Point out each Plasmodium parasite.
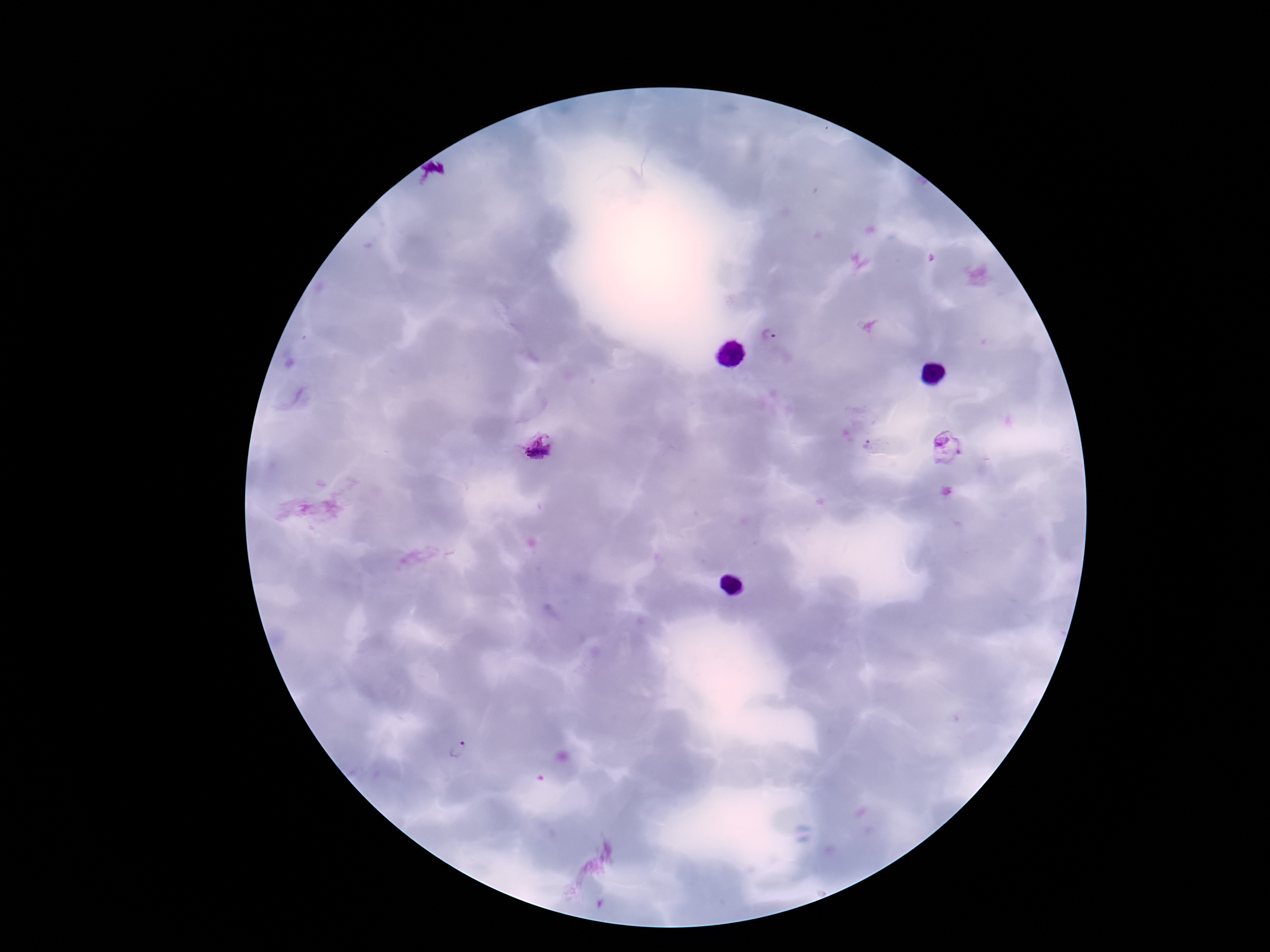
Approximate centers as {x, y} in pixels.
Plasmodium parasites: {770, 335}, {870, 446}, {538, 447}, {947, 449}, {459, 748}.

Summary:
  - Image size: 1270×952 pixels
  - Field of view: one from this slide
  - Capture: smartphone camera through the microscope eyepiece
  - Magnification: 100x
  - Preparation: thick blood film
  - Stain: Giemsa
  - Patient malaria status: positive